Classify this cell by malaria status.
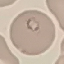
Parasitized.

Summary:
  - Capture: smartphone through the microscope eyepiece
  - Preparation: thin blood film
  - Image type: cell patch, automatically extracted from a larger field of view and resized to 64 × 64 pixels
  - Stain: Giemsa